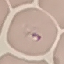

malaria status = parasitized
stain = Giemsa
capture = smartphone through the microscope eyepiece
preparation = thin blood film
image type = cell patch, automatically extracted from a larger field of view and resized to 64 × 64 pixels